Identify the preparation type.
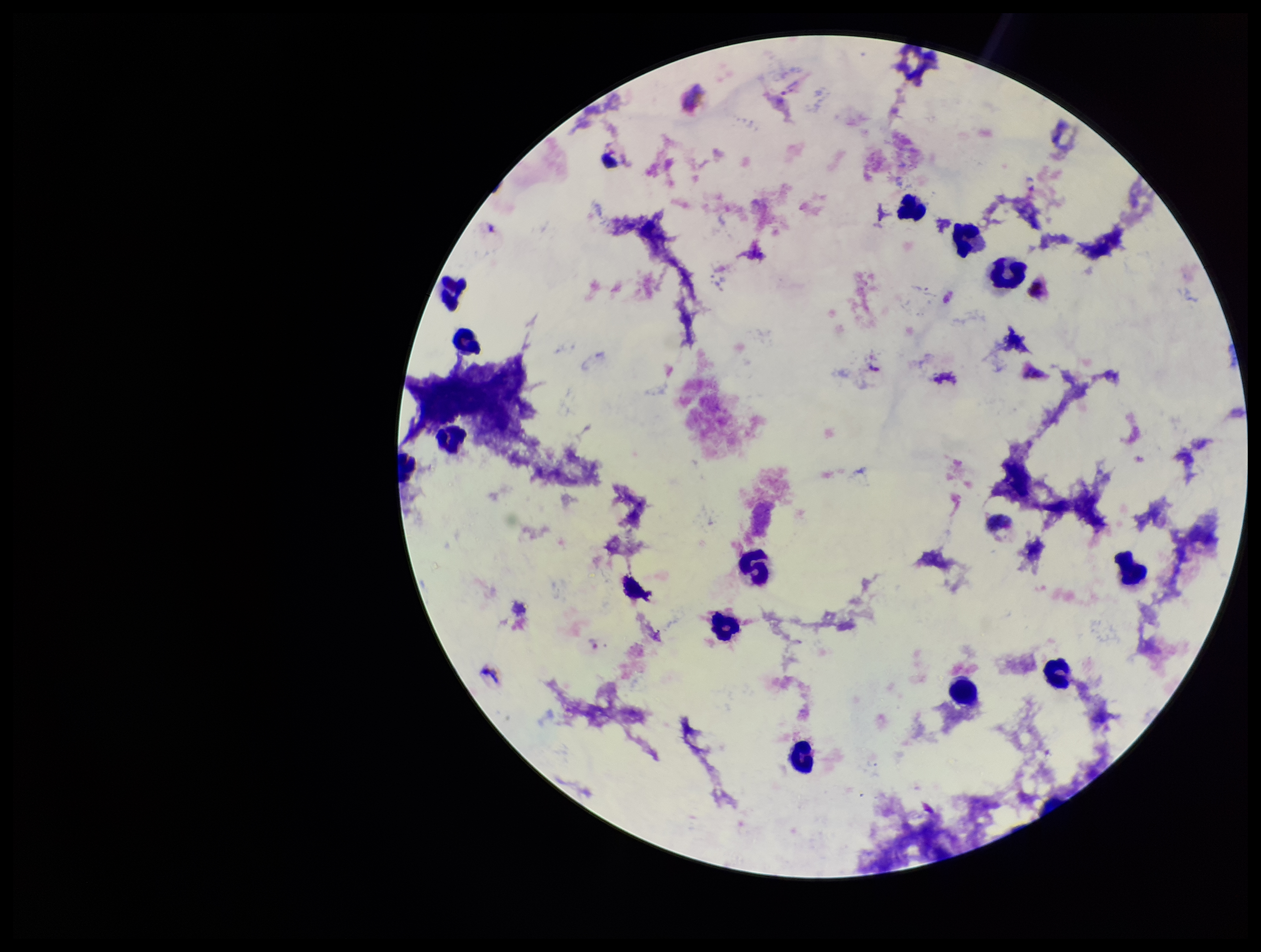
A thick smear.

parasite_count: 2
leukocyte_count: 14
field_of_view: single
patient_malaria_status: positive
stain: Giemsa
plasmodium_parasites: seen
capture: smartphone photograph through the microscope eyepiece
species_reported_for_this_patient: Plasmodium vivax
image_size: 1261×952 pixels